Give the position of every malaria parasite.
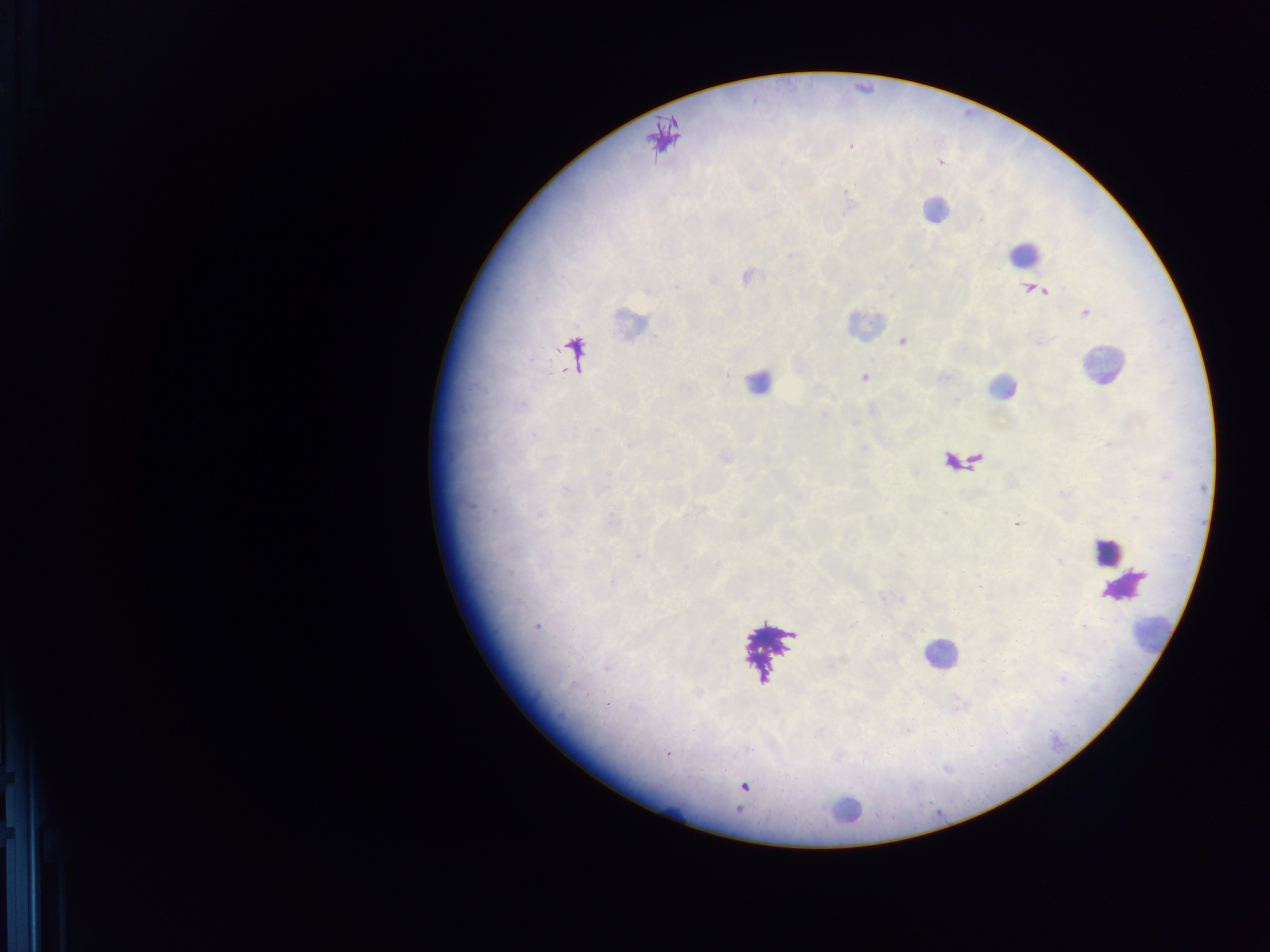
Approximate centers as {x, y} in pixels.
Malaria parasites: {851, 146}, {939, 162}, {790, 255}, {747, 276}, {1034, 290}, {1085, 312}, {902, 341}, {864, 377}, {725, 457}, {1016, 524}, {661, 527}, {638, 556}, {536, 627}, {606, 668}, {668, 754}, {743, 786}.

Summary:
  - Leukocyte locations: {934, 210}, {1024, 254}, {631, 324}, {863, 324}, {1102, 366}, {758, 382}, {1002, 387}, {963, 461}, {1105, 551}, {1125, 585}, {1157, 636}, {940, 654}, {845, 810}
  - Image size: 1270×952 pixels
  - Field of view: single
  - Preparation: thick blood smear
  - Capture: mobile-phone photograph through a microscope
  - Country: Ghana